Assess this cell for malaria.
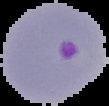
Parasitized.

preparation: thin blood smear
image_size: 109×106 pixels
image_type: segmented cell region with the area outside set to black